Identify the parasite.
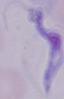

A trypanosome.

Summary:
  - Magnification: 1000x
  - Modality: photomicrograph